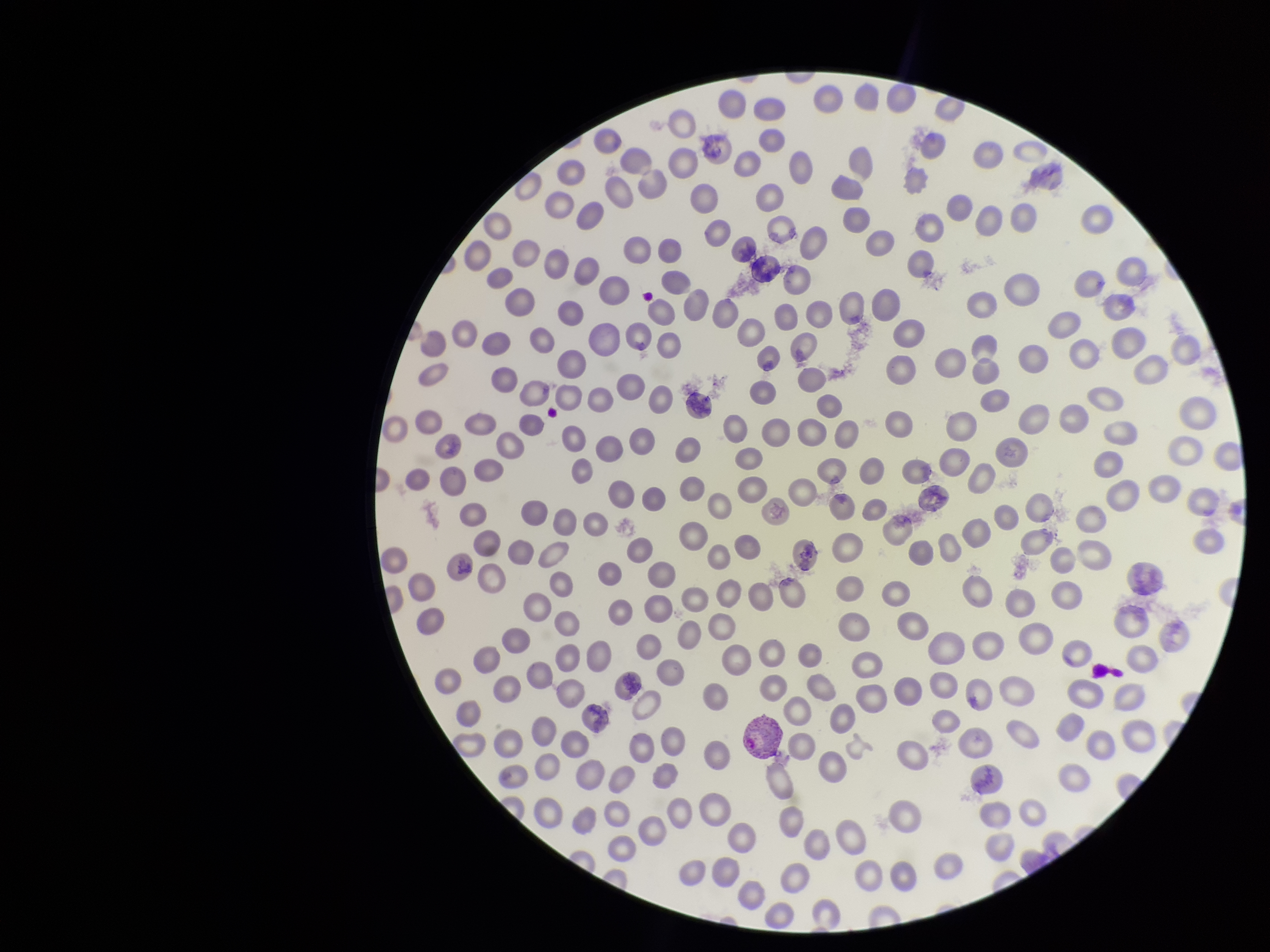

parasitized_red_blood_cells: detected
field_of_view: single
image_size: 1270×952 pixels
red_blood_cell_count: 267
parasitized_red_blood_cell_count: 1
preparation: thin blood smear
capture: smartphone photograph through the microscope eyepiece
patient_malaria_status: infected
stain: Giemsa
species_reported_for_this_patient: Plasmodium vivax